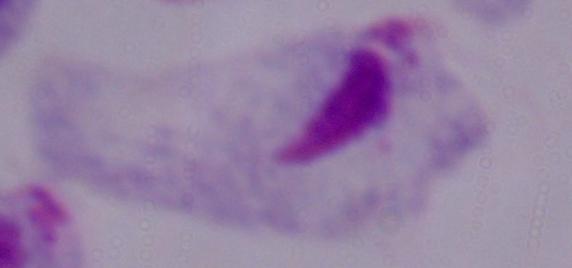

1000x magnification. Photomicrograph. A trichomonad is seen.